Identify the parasite.
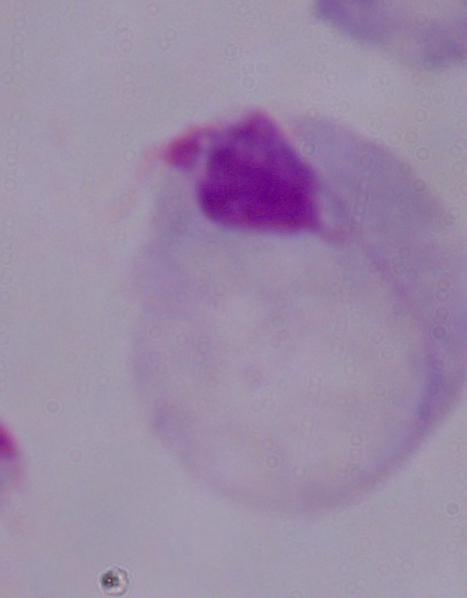

A trichomonad.

magnification: 1000x
modality: photomicrograph